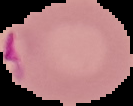
image type = segmented cell region on a black background
image size = 133×106 pixels
preparation = thin blood smear
malaria status = parasitized